Locate every blood parasite and identify its species.
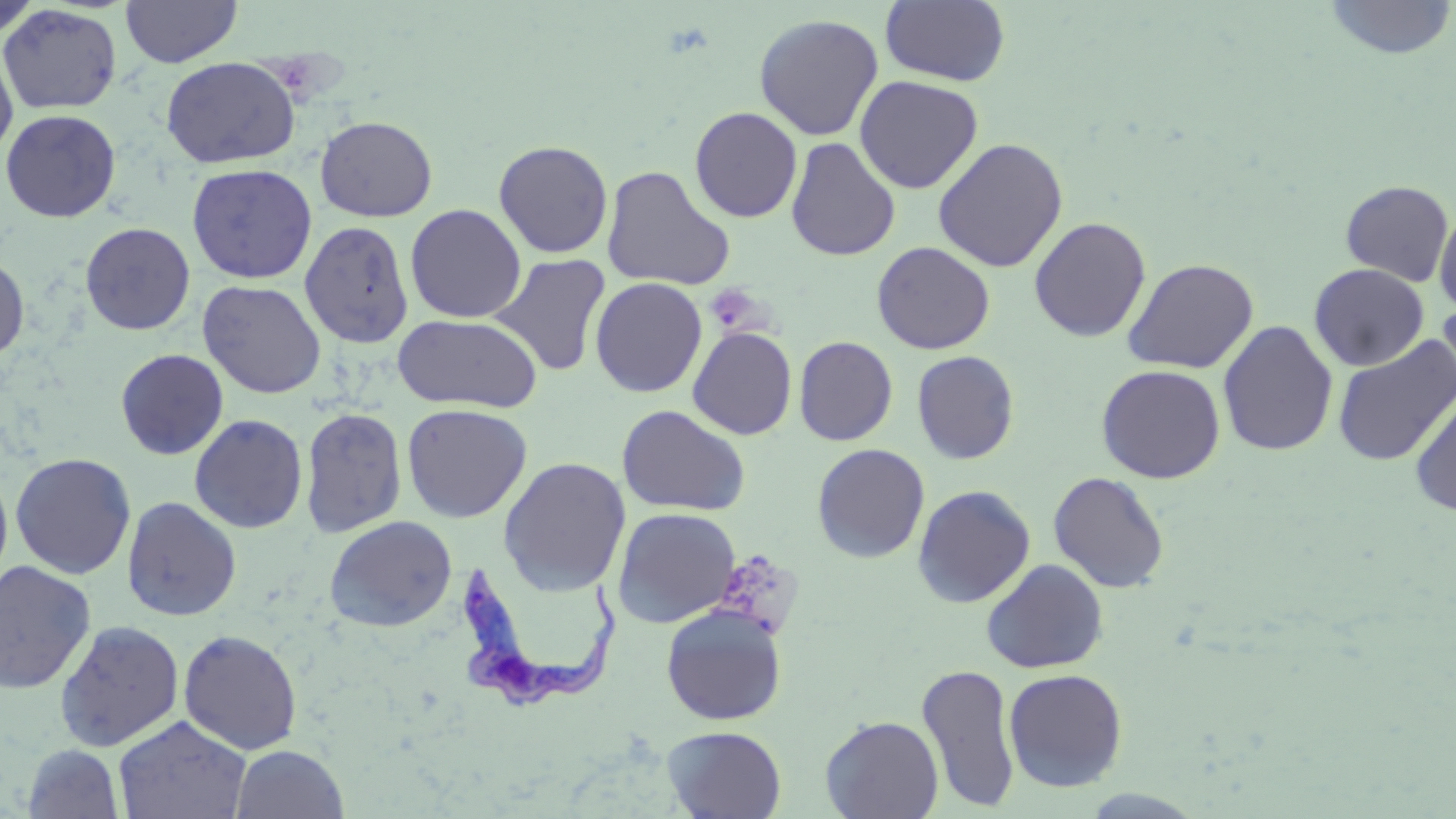

Approximate bounding boxes as (x1, y1, x2, y2) in pixels.
Trypanosoma brucei: (460, 554, 630, 715).
No Plasmodium falciparum, Plasmodium ovale, Plasmodium malariae, Plasmodium vivax, or Babesia divergens observed.

slide-level diagnosis = Trypanosoma brucei
modality = light microscopy
stain = May-Grünwald-Giemsa
platelet locations = approximate bounding boxes as (x1, y1, x2, y2) in pixels: (706, 284, 764, 334), (707, 550, 806, 642)
preparation = thin blood film
uninfected red blood cell locations = approximate bounding boxes as (x1, y1, x2, y2) in pixels: (0, 0, 40, 42), (121, 0, 242, 67), (880, 0, 1010, 86), (1322, 0, 1456, 60), (0, 4, 123, 114), (754, 13, 884, 141), (0, 43, 18, 163), (161, 56, 300, 168), (854, 75, 983, 194), (689, 106, 803, 223), (1, 109, 121, 222), (315, 116, 437, 222), (785, 137, 901, 261), (932, 137, 1069, 272), (493, 140, 613, 258), (186, 163, 318, 284), (601, 165, 735, 292), (1340, 179, 1454, 286), (405, 204, 526, 323), (1434, 205, 1456, 317), (1028, 217, 1151, 343), (299, 221, 414, 348), (80, 222, 195, 335), (871, 241, 995, 354), (491, 254, 611, 376), (0, 255, 30, 360), (1122, 258, 1258, 374), (1309, 263, 1429, 371), (590, 277, 707, 398), (197, 280, 326, 398), (1436, 295, 1456, 405), (649, 302, 773, 423), (392, 314, 542, 413), (1217, 320, 1338, 457), (687, 326, 797, 440), (1332, 335, 1456, 466), (794, 336, 897, 446), (115, 348, 228, 460), (911, 350, 1019, 464), (1095, 364, 1226, 484), (1409, 385, 1456, 516), (401, 403, 532, 523), (616, 405, 750, 517), (300, 406, 407, 538), (189, 413, 308, 534), (811, 443, 930, 563), (10, 452, 136, 580), (497, 456, 632, 595), (0, 464, 13, 588), (1048, 471, 1170, 593), (912, 485, 1036, 608), (121, 496, 241, 621), (611, 507, 741, 628), (324, 515, 457, 632), (981, 559, 1109, 674), (0, 560, 97, 694), (661, 605, 787, 725), (54, 620, 185, 752), (178, 629, 303, 755), (916, 662, 1020, 812), (1003, 668, 1128, 792), (820, 714, 943, 819), (112, 715, 251, 819), (662, 725, 787, 819), (21, 744, 125, 819), (230, 744, 349, 818)
image size = 1456×819 pixels
field of view = one of a larger specimen
magnification = 1000x